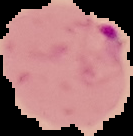

The area outside the segmented cell region is set to black. Image is 133×136 pixels. From a thin blood film. Malaria status: parasitized.